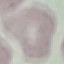
Summary:
  - Malaria status: uninfected
  - Stain: Giemsa
  - Preparation: thin smear
  - Capture: smartphone through the microscope eyepiece
  - Image type: automatically extracted cell patch, resized to 64 × 64 pixels